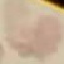
Summary:
  - Malaria status: uninfected
  - Stain: Giemsa
  - Image type: cell patch, automatically extracted from a larger field of view and resized to 64 × 64 pixels
  - Capture: smartphone camera at the microscope eyepiece
  - Preparation: thin smear